Give the preparation type.
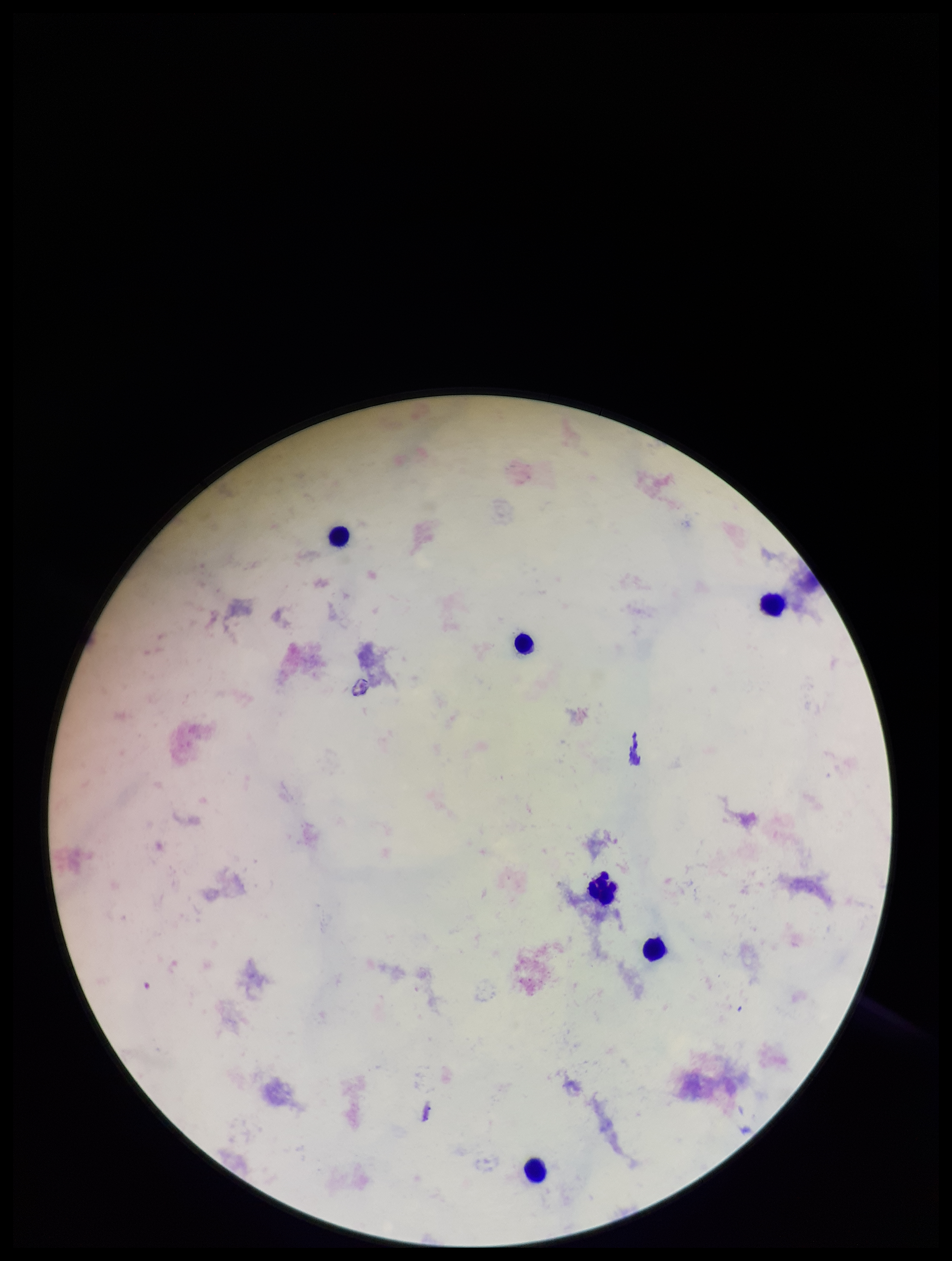

Thick.

stain = Giemsa
patient malaria status = negative
leukocyte count = 6
image size = 952×1261 pixels
parasite count = 0
field of view = one from this slide
Plasmodium parasites = none detected
capture = smartphone photograph through the microscope eyepiece